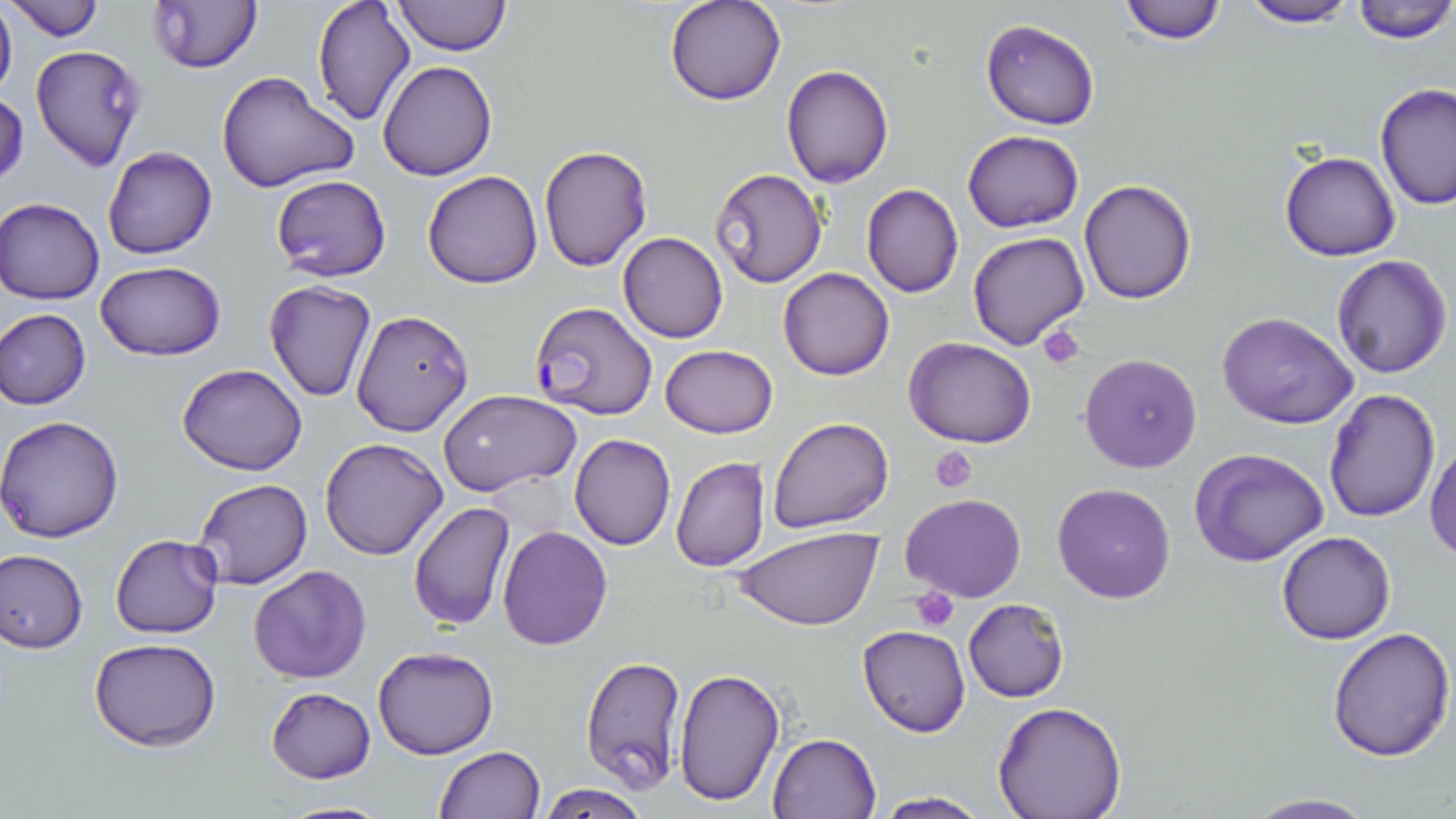
{
  "slide_level_diagnosis": "Plasmodium falciparum",
  "magnification": "1000x",
  "preparation": "thin blood film",
  "image_size": "1456×819 pixels",
  "plasmodium_falciparum_infected_red_blood_cell_locations": "approximate bounding boxes as (x1,y1)-(x2,y2) corner pairs in pixels: (529,301)-(657,420)",
  "platelet_locations": "approximate bounding boxes as (x1,y1)-(x2,y2) corner pairs in pixels: (1039,325)-(1086,369), (930,446)-(978,494), (910,586)-(959,631)",
  "field_of_view": "single",
  "stain": "May-Grünwald-Giemsa",
  "modality": "light microscopy",
  "uninfected_red_blood_cell_locations": "approximate bounding boxes as (x1,y1)-(x2,y2) corner pairs in pixels: (0,0)-(18,101), (3,0)-(105,41), (393,0)-(511,55), (664,0)-(785,106), (1115,0)-(1230,46), (1239,0)-(1358,28), (1348,0)-(1456,42), (146,1)-(264,74), (310,1)-(417,128), (980,19)-(1101,130), (31,44)-(146,173), (377,59)-(496,180), (782,64)-(894,186), (217,71)-(360,194), (1373,84)-(1456,211), (0,90)-(28,191), (962,130)-(1085,233), (538,144)-(652,271), (102,145)-(217,259), (1280,149)-(1401,261), (711,167)-(828,287), (423,171)-(542,290), (270,173)-(392,281), (1078,178)-(1196,303), (862,184)-(964,297), (1,198)-(104,304), (966,231)-(1089,350), (619,232)-(728,342), (1331,253)-(1452,377), (96,261)-(224,361), (778,267)-(895,380), (263,281)-(378,403), (0,309)-(91,410), (350,309)-(473,437), (1216,311)-(1358,429), (904,337)-(1036,448), (660,345)-(777,437), (1078,352)-(1204,475), (177,363)-(308,475), (1322,386)-(1439,523), (439,390)-(580,495), (0,415)-(124,542), (768,417)-(893,534), (569,433)-(676,550), (320,436)-(449,560), (1426,439)-(1456,562), (1191,448)-(1331,566), (670,456)-(770,572), (190,478)-(312,590), (1053,481)-(1177,603), (901,493)-(1024,603), (408,501)-(514,631), (497,525)-(612,649), (735,529)-(881,631), (1277,531)-(1395,645), (110,534)-(225,638), (0,547)-(89,653), (248,564)-(371,683), (964,598)-(1068,702), (858,624)-(969,736), (1328,626)-(1455,762), (89,637)-(221,751), (373,646)-(499,759), (580,654)-(687,793), (673,666)-(786,808), (266,687)-(375,783), (993,701)-(1127,819), (768,733)-(879,819), (432,746)-(544,819), (536,782)-(650,819), (874,792)-(990,818), (1244,792)-(1376,818), (277,800)-(395,818)"
}